Name the parasite shown.
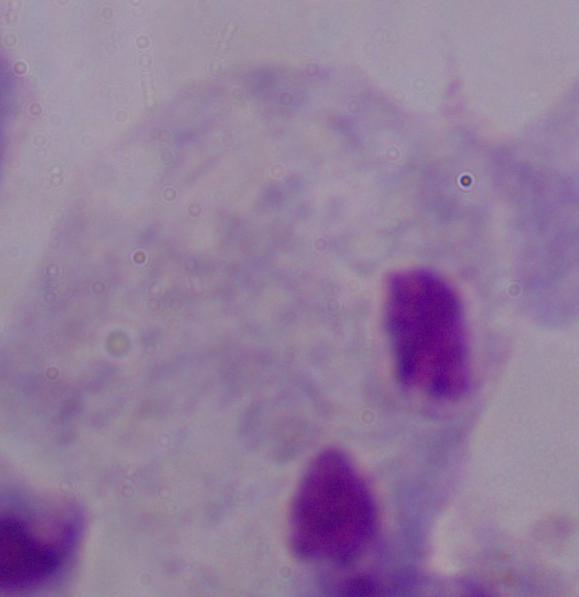
This is a trichomonad.

Photomicrograph. 1000x magnification.